Identify the blood parasite species.
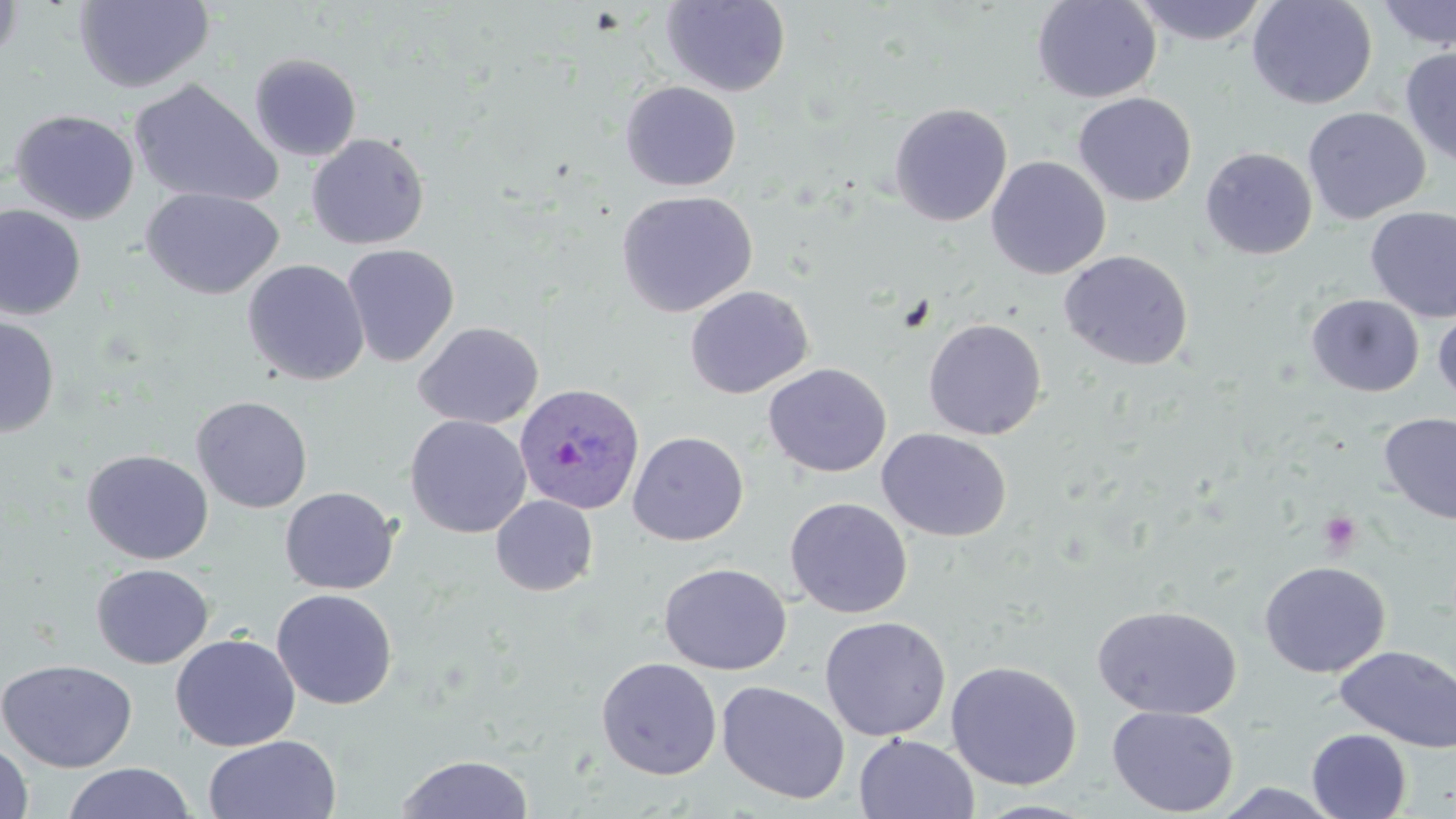

Plasmodium ovale.

Summary:
  - Coordinate format: approximate bounding boxes as (x1,y1)-(x2,y2) corner pairs in pixels
  - Plasmodium ovale-infected red blood cell locations: (513,382)-(646,515)
  - Uninfected red blood cell locations: (0,0)-(24,65), (1031,0)-(1162,103), (1132,0)-(1271,46), (1247,0)-(1378,110), (74,1)-(214,93), (660,1)-(791,97), (1374,1)-(1456,51), (1400,45)-(1456,168), (248,52)-(363,162), (128,79)-(282,208), (619,81)-(741,191), (1072,92)-(1197,207), (889,103)-(1013,227), (1302,107)-(1430,225), (9,109)-(140,225), (306,133)-(430,250), (1200,147)-(1318,260), (986,156)-(1111,280), (142,187)-(283,299), (616,189)-(758,318), (0,205)-(86,321), (1365,206)-(1456,323), (341,243)-(460,367), (1058,250)-(1194,371), (242,259)-(370,386), (684,285)-(813,399), (1305,294)-(1424,397), (1433,307)-(1456,407), (0,317)-(60,438), (923,318)-(1047,440), (413,321)-(544,429), (763,363)-(892,478), (191,395)-(313,513), (1377,412)-(1456,525), (404,415)-(532,538), (876,428)-(1012,542), (627,431)-(749,546), (81,449)-(213,565), (279,486)-(400,595), (490,494)-(599,596), (785,497)-(913,619), (1258,561)-(1391,678), (658,562)-(793,675), (90,563)-(214,669), (271,588)-(398,709), (1091,604)-(1242,720), (819,616)-(951,741), (170,633)-(301,752), (1335,645)-(1456,753), (595,657)-(722,780), (0,658)-(138,773), (945,660)-(1083,791), (716,680)-(850,804), (1107,705)-(1239,816), (1306,729)-(1411,818), (853,733)-(980,819), (203,734)-(342,819), (0,739)-(33,819), (395,753)-(534,818), (62,762)-(195,819), (1211,783)-(1349,818), (972,799)-(1102,818)
  - Platelet locations: (1318,511)-(1363,555)
  - Image size: 1456×819 pixels
  - Preparation: thin blood film
  - Field of view: one of a larger specimen
  - Magnification: 1000x
  - Modality: optical microscopy
  - Stain: May-Grünwald-Giemsa